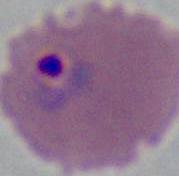

A Plasmodium parasite is shown. Captured at either 400x or 1000x magnification. Photomicrograph.